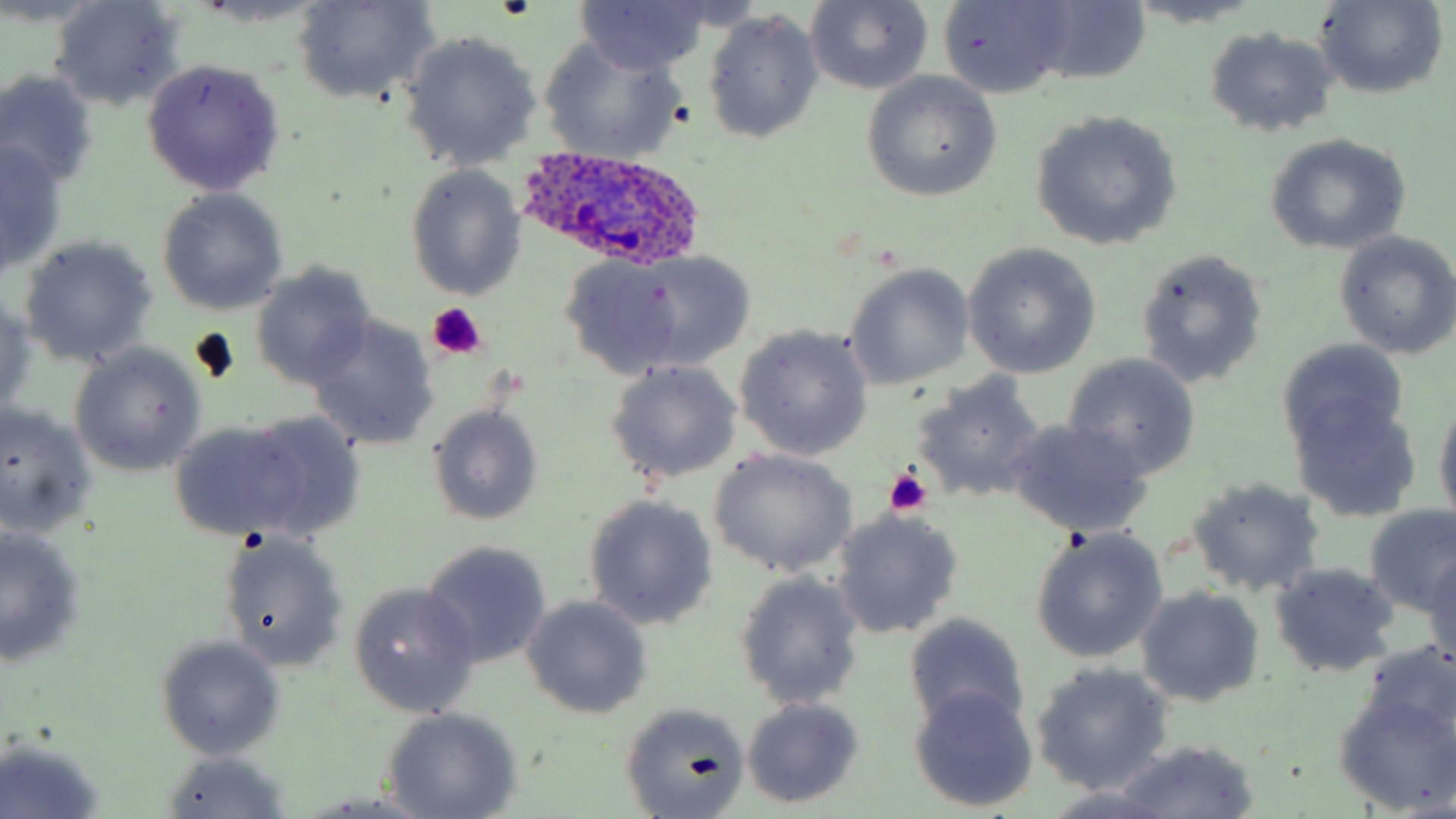

Approximate bounding boxes as (x1,y1)-(x2,y2) corner pairs in pixels. Plasmodium ovale-infected red blood cell locations: (518,143)-(708,272). Uninfected red blood cell locations: (291,0)-(440,107), (574,0)-(710,74), (1311,0)-(1449,101), (48,1)-(184,113), (804,1)-(933,95), (0,2)-(105,30), (940,2)-(1072,99), (1021,2)-(1153,87), (1126,2)-(1265,30), (701,10)-(824,145), (77,18)-(238,163), (1205,26)-(1340,139), (399,30)-(543,172), (539,37)-(689,163), (141,57)-(286,196), (0,71)-(101,189), (862,73)-(1001,200), (1029,111)-(1182,251), (1262,134)-(1412,256), (0,140)-(67,276), (405,166)-(527,301), (156,190)-(290,315), (1332,231)-(1456,360), (18,234)-(157,367), (962,244)-(1101,378), (1135,247)-(1269,388), (619,250)-(758,370), (560,255)-(698,377), (250,263)-(377,390), (842,263)-(975,391), (0,290)-(37,417), (306,315)-(437,452), (735,325)-(873,460), (1277,337)-(1410,462), (70,344)-(206,477), (1062,355)-(1202,480), (605,360)-(742,484), (910,373)-(1047,505), (1289,394)-(1420,523), (1433,398)-(1456,523), (0,403)-(99,539), (426,404)-(545,525), (228,411)-(368,542), (167,418)-(318,541), (1002,420)-(1154,538), (707,449)-(856,578), (1187,477)-(1325,598), (583,494)-(717,632), (1361,505)-(1456,619), (831,509)-(963,639), (0,528)-(86,668), (1029,528)-(1169,664), (215,529)-(351,670), (419,539)-(554,668), (1424,553)-(1456,672), (1267,561)-(1401,679), (734,570)-(866,709), (348,582)-(482,715), (1136,587)-(1264,709), (520,595)-(653,720), (904,612)-(1030,736), (154,634)-(286,759), (1030,663)-(1173,796), (1331,680)-(1456,813), (908,688)-(1039,812), (740,696)-(866,808), (618,701)-(750,819), (381,710)-(523,819), (1,737)-(107,818), (1111,740)-(1258,819), (156,750)-(294,818), (1041,789)-(1180,819), (303,791)-(443,816). Platelet locations: (426,302)-(488,362), (884,468)-(932,516). Slide-level diagnosis: Plasmodium ovale. Optical microscopy. Thin blood smear. Captured at 1000x magnification. May-Grünwald-Giemsa-stained preparation. Single field of view. Image is 1456×819 pixels.